Name the parasite shown.
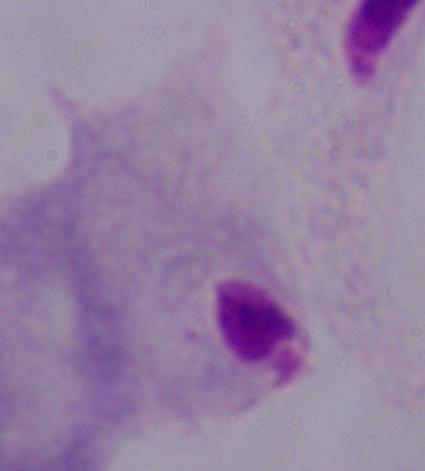

A trichomonad.

Micrograph. Captured at 1000x magnification.